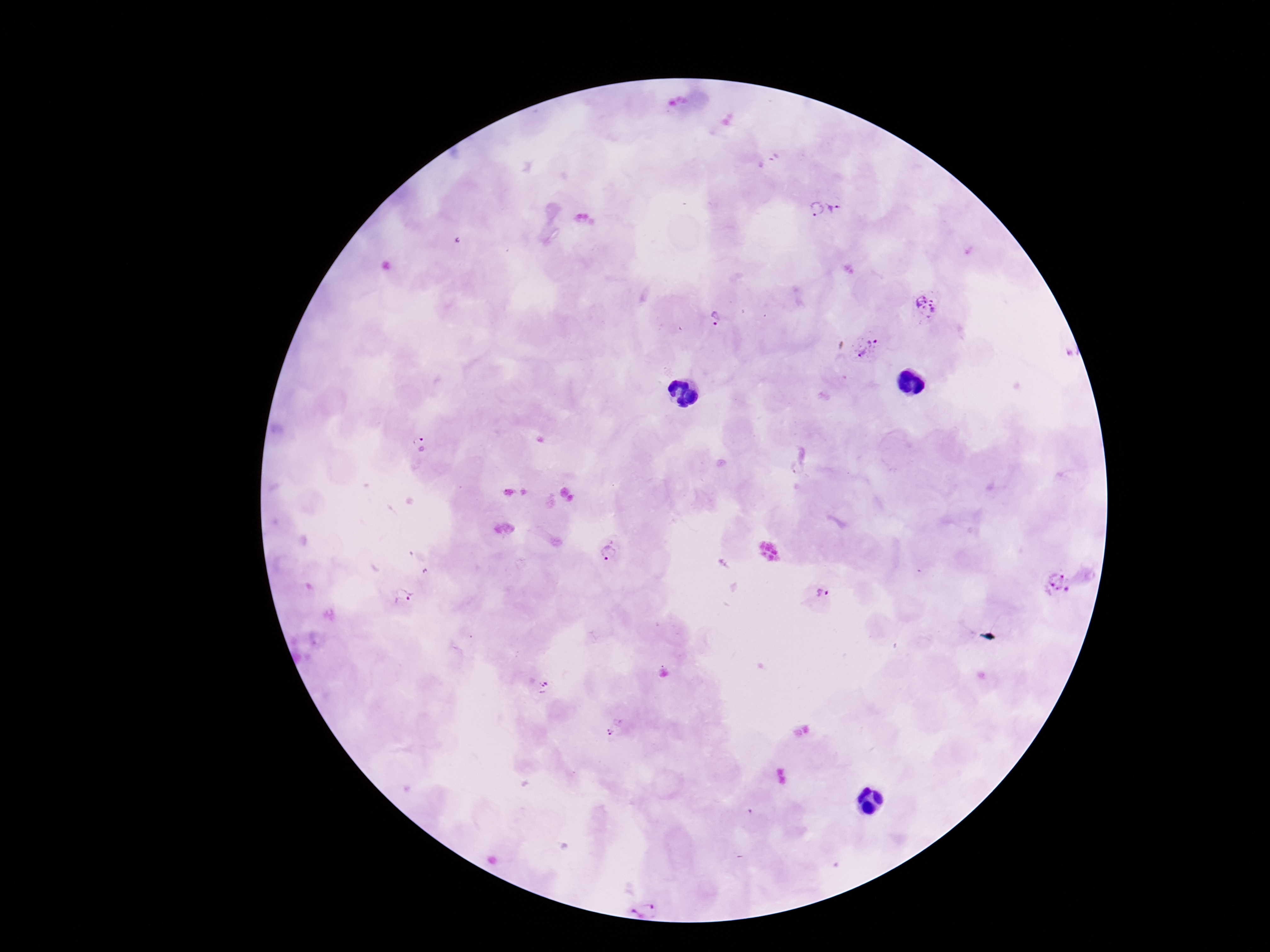

Approximate object centers, in pixels from the top-left corner.
Summary:
  - Plasmodium parasite locations: (x=837, y=205), (x=814, y=210), (x=926, y=303), (x=716, y=317), (x=867, y=347), (x=420, y=444), (x=609, y=552), (x=1058, y=584), (x=822, y=593), (x=403, y=596), (x=546, y=686), (x=609, y=733), (x=641, y=904)
  - Stain: Giemsa
  - Image size: 1270×952 pixels
  - Capture: smartphone camera through the microscope eyepiece
  - Patient malaria status: positive
  - Magnification: 100x
  - Preparation: thick blood film
  - Field of view: one from this slide